Describe the morphology of the red blood cells.
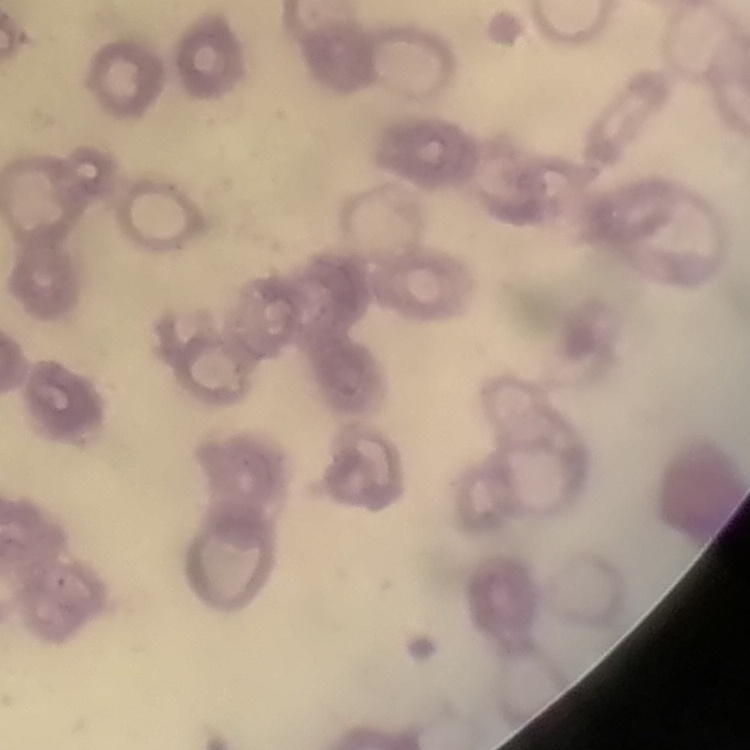

Rouleaux formation.

Field's or Giemsa stain. Thin peripheral smear. One tile cut from a larger photomicrograph.